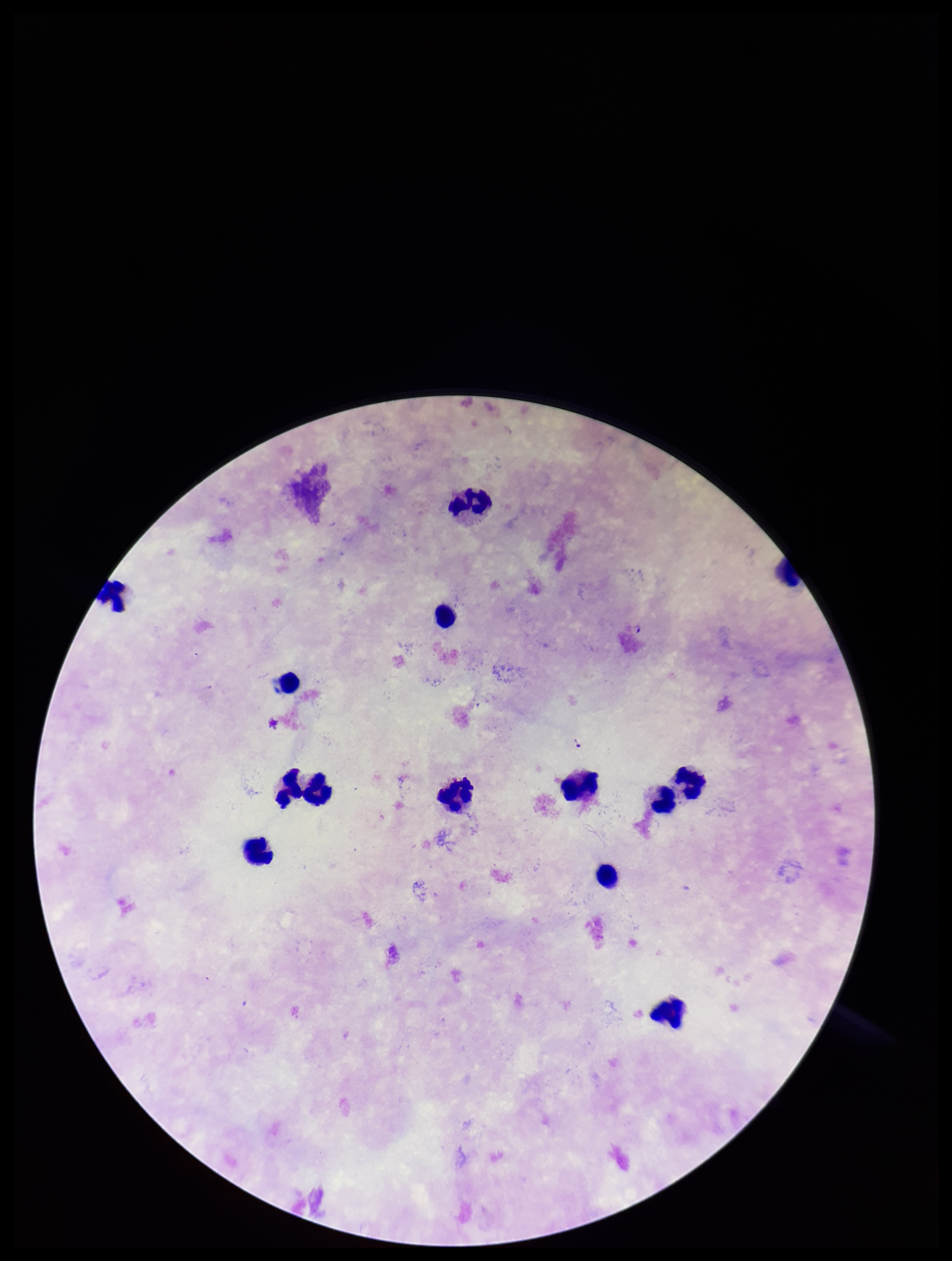
leukocyte count = 14
image size = 952×1261 pixels
capture = smartphone photograph through the microscope eyepiece
preparation = thick
species reported for this patient = Plasmodium falciparum
field of view = one from this slide
Plasmodium parasites = none seen
patient malaria status = infected
stain = Giemsa
parasite count = 0